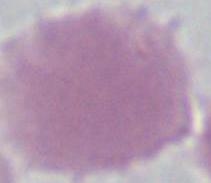
Summary:
  - Identification: erythrocyte
  - Modality: micrograph
  - Magnification: 1000x